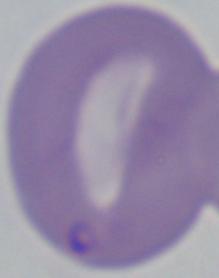

modality: photomicrograph
magnification: 1000x
identification: Babesia